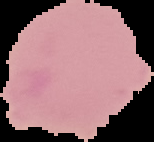 The area outside the segmented cell region is set to black. From a thin blood film. Image is 154×142 pixels. Malaria status: uninfected.